Name the blood parasite species.
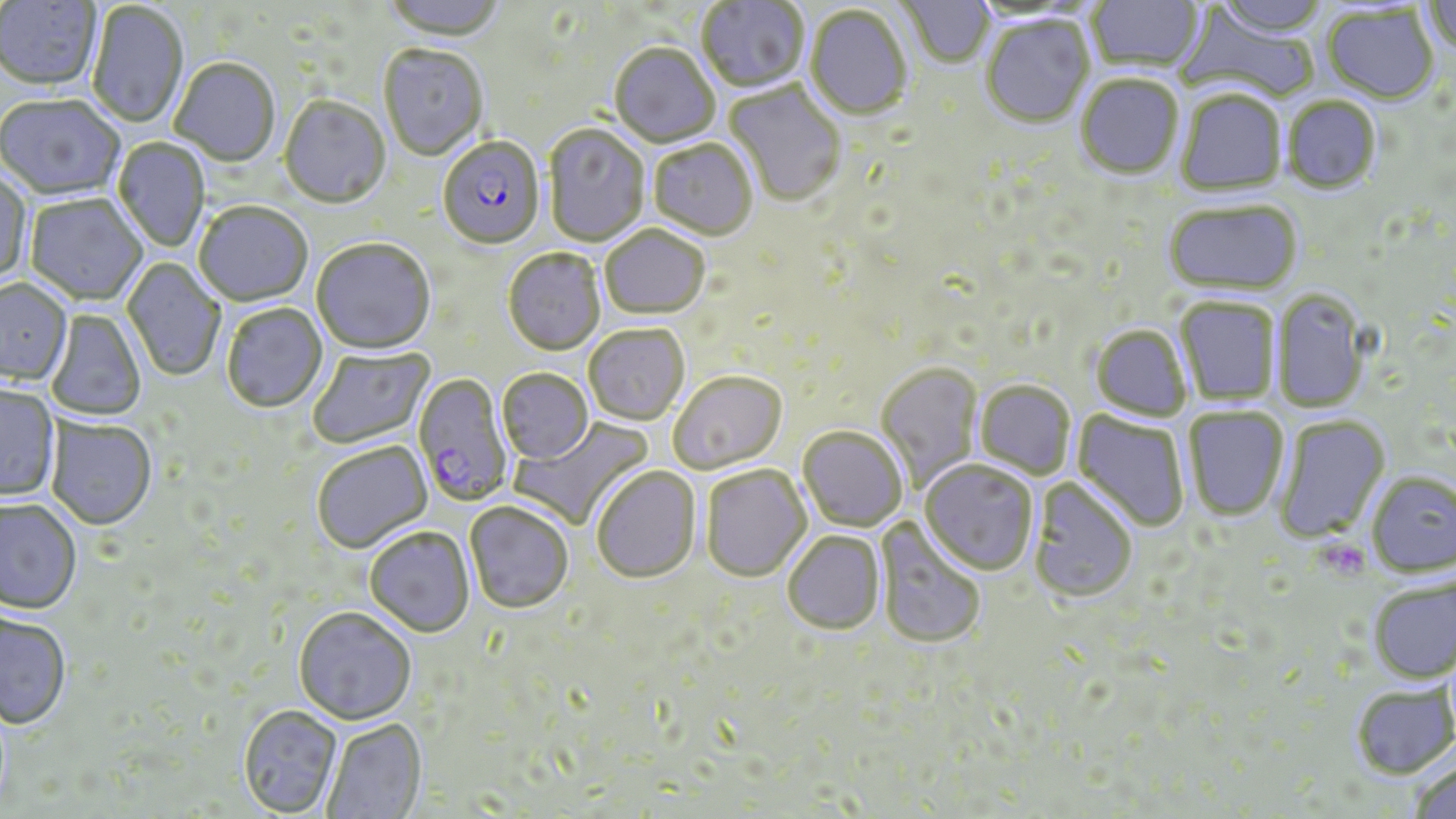
Plasmodium falciparum.

Summary:
  - Coordinate format: approximate bounding boxes as (x1, y1, x2, y2) in pixels
  - Uninfected red blood cell locations: (0, 0, 101, 94), (379, 0, 507, 45), (697, 0, 809, 94), (896, 0, 994, 70), (1087, 0, 1204, 75), (1213, 0, 1328, 39), (1423, 0, 1456, 56), (87, 3, 188, 129), (1323, 4, 1439, 104), (805, 6, 912, 122), (1176, 7, 1321, 105), (981, 18, 1095, 129), (609, 45, 720, 149), (378, 46, 488, 162), (170, 59, 281, 167), (1075, 76, 1184, 182), (723, 80, 847, 208), (1176, 90, 1287, 198), (0, 96, 125, 203), (1282, 96, 1381, 194), (279, 97, 391, 211), (543, 124, 650, 248), (113, 138, 210, 252), (648, 141, 758, 242), (0, 170, 32, 286), (24, 194, 148, 308), (1164, 200, 1302, 295), (194, 204, 313, 308), (600, 227, 710, 322), (311, 241, 435, 356), (502, 250, 606, 357), (122, 258, 226, 382), (0, 279, 73, 388), (1271, 288, 1370, 414), (1176, 296, 1281, 407), (221, 304, 328, 414), (45, 309, 147, 421), (1090, 325, 1192, 422), (584, 326, 690, 427), (308, 346, 436, 450), (875, 363, 983, 493), (496, 370, 593, 465), (669, 373, 788, 476), (974, 381, 1076, 479), (0, 385, 60, 502), (1183, 406, 1289, 520), (1072, 410, 1190, 532), (1274, 414, 1389, 543), (511, 415, 655, 530), (45, 418, 157, 532), (798, 428, 906, 532), (312, 443, 433, 555), (920, 461, 1039, 576), (701, 466, 811, 584), (591, 467, 702, 585), (1366, 471, 1456, 577), (1029, 479, 1137, 605), (1, 500, 82, 617), (464, 502, 574, 617), (875, 517, 986, 651), (365, 529, 475, 639), (783, 532, 884, 636), (1368, 576, 1456, 683), (293, 609, 416, 727), (0, 612, 71, 731), (1352, 684, 1455, 778), (238, 707, 343, 817), (321, 720, 428, 819), (1409, 757, 1456, 819)
  - Plasmodium falciparum-infected red blood cell locations: (434, 131, 542, 255), (413, 374, 514, 508)
  - Platelet locations: (1318, 539, 1370, 581)
  - Image size: 1456×819 pixels
  - Field of view: single
  - Modality: light microscopy
  - Magnification: 1000x
  - Preparation: thin blood film
  - Stain: May-Grünwald-Giemsa